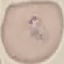

result: malaria parasites identified
preparation: thin smear
stain: Giemsa
image_type: automatically extracted cell patch, resized to 64 × 64 pixels
capture: smartphone through the microscope eyepiece